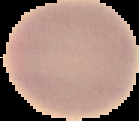

Malaria status: uninfected. Cell region segmented out of the field of view; the surrounding area is masked to black. From a thin blood film. Image is 139×121 pixels.